Identify the blood parasite species.
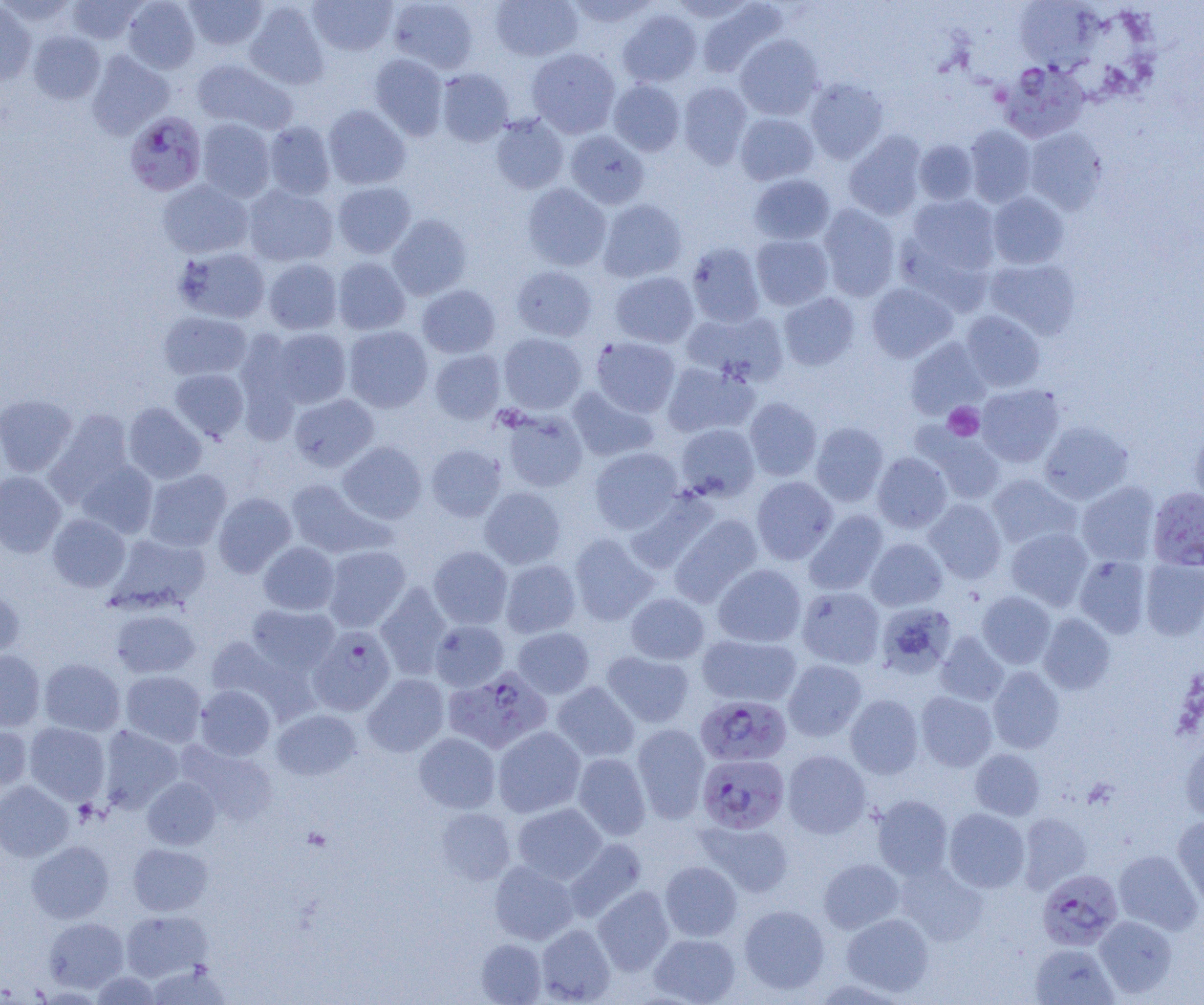
Plasmodium falciparum.

Summary:
  - Coordinate format: approximate bounding boxes as (x1,y1)-(x2,y2) corner pairs in pixels
  - Platelet locations: (943,402)-(984,441)
  - Plasmodium falciparum-infected red blood cell locations (subset): (1000,62)-(1090,143), (124,111)-(207,196), (1148,487)-(1204,571), (308,626)-(396,716), (443,667)-(552,754), (695,695)-(792,767), (697,754)-(789,834)
  - Uninfected red blood cell locations (subset): (122,0)-(200,74), (184,0)-(268,50), (308,0)-(397,56), (387,0)-(479,73), (491,0)-(583,61), (565,0)-(658,28), (65,1)-(146,44), (243,1)-(330,89), (1015,1)-(1097,71), (0,2)-(37,85), (696,2)-(786,78), (617,8)-(703,87), (28,30)-(105,104), (734,34)-(823,120), (527,48)-(620,138), (86,50)-(174,139), (369,54)-(448,140), (192,58)-(298,135), (436,68)-(514,146), (804,78)-(889,164), (608,80)-(685,156), (678,81)-(752,168), (323,104)-(411,190), (735,113)-(819,185), (491,114)-(569,194), (196,118)-(276,202), (263,121)-(336,199), (964,125)-(1037,207), (1024,127)-(1107,214), (565,130)-(650,209), (844,131)-(927,221), (914,140)-(978,205), (749,173)-(835,245), (158,179)-(253,258), (332,182)-(416,258), (522,183)-(612,271), (243,184)-(338,267), (987,192)-(1069,269), (906,194)-(1001,276), (597,199)-(687,282), (818,204)-(901,301), (387,213)-(472,300), (751,234)-(834,310), (685,242)-(765,327), (175,246)-(271,323), (332,257)-(411,335), (263,258)-(342,334), (985,258)-(1081,339), (511,265)-(598,341), (610,271)-(699,348), (866,283)-(957,363), (417,284)-(501,358), (778,292)-(860,371), (682,309)-(788,386), (960,310)-(1045,392), (159,311)-(252,380), (344,326)-(432,412), (265,328)-(352,409), (498,333)-(586,414), (591,337)-(681,417), (905,337)-(990,419), (430,349)-(505,424), (661,361)-(757,438), (170,368)-(249,441), (976,384)-(1064,467), (567,386)-(658,461), (0,394)-(77,477), (289,394)-(379,472), (744,397)-(822,481), (123,402)-(206,484), (498,408)-(588,492), (45,409)-(134,505), (1039,420)-(1133,504), (811,422)-(889,506), (676,423)-(760,501), (1190,424)-(1204,509), (919,429)-(1006,504), (337,441)-(426,524), (426,444)-(506,521), (589,447)-(683,534), (872,452)-(953,532), (76,460)-(158,538), (144,469)-(231,551), (0,471)-(66,557), (987,474)-(1081,549), (752,476)-(838,564), (285,479)-(389,559), (1076,481)-(1160,566), (480,486)-(566,569), (625,490)-(718,574), (213,493)-(296,578), (924,498)-(1006,583), (804,510)-(888,595), (48,514)-(130,592), (669,514)-(763,607), (1007,527)-(1093,610), (107,533)-(209,613), (569,534)-(658,625), (866,538)-(947,611), (258,542)-(339,615), (322,545)-(410,632), (428,546)-(512,629), (1074,555)-(1152,638), (1140,558)-(1204,640), (500,560)-(580,638), (713,564)-(806,647), (375,582)-(453,679), (797,586)-(885,668), (0,588)-(24,661), (977,591)-(1055,668), (626,593)-(710,664), (875,602)-(956,678), (246,604)-(340,676), (110,609)-(201,678), (1039,613)-(1115,694), (430,620)-(508,691), (513,627)-(594,698), (935,631)-(1009,706), (697,633)-(801,706), (204,635)-(311,720), (0,649)-(46,731), (602,651)-(695,728), (39,658)-(125,736), (783,659)-(867,741), (988,666)-(1065,753), (121,670)-(206,747), (363,674)-(449,757), (552,681)-(640,762), (195,685)-(275,760), (916,691)-(997,771), (845,694)-(924,778), (272,709)-(361,780), (24,722)-(110,805), (0,723)-(32,794), (632,724)-(710,822), (97,725)-(183,812), (492,726)-(586,817), (414,733)-(500,813), (1180,741)-(1204,823), (178,742)-(278,825), (969,749)-(1045,820), (782,750)-(871,838), (572,753)-(651,840), (142,777)-(220,849), (0,781)-(74,861), (872,795)-(953,879), (512,803)-(607,884), (435,807)-(515,885), (943,808)-(1029,892), (1018,812)-(1092,893), (1172,816)-(1204,908), (698,820)-(794,897), (564,838)-(647,922), (26,840)-(114,924), (128,843)-(213,915), (1113,850)-(1202,934), (819,858)-(904,934), (489,860)-(578,944), (660,861)-(742,942), (895,863)-(988,946), (592,886)-(675,975), (739,905)-(830,994), (120,910)-(212,981), (841,913)-(934,996), (1094,915)-(1178,998), (43,916)-(129,993), (535,924)-(615,1004), (649,933)-(740,1004), (476,939)-(546,1004), (1029,943)-(1118,1004), (146,963)-(231,1004), (92,972)-(163,1005), (811,977)-(911,1005)
  - Field of view: single
  - Image size: 1204×1005 pixels
  - Preparation: thin blood smear
  - Magnification: 1000x
  - Modality: optical microscopy